Classify this cell by malaria status.
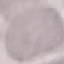

It is uninfected.

Summary:
  - Stain: Giemsa
  - Capture: smartphone camera at the microscope eyepiece
  - Preparation: thin blood smear
  - Image type: automatically extracted cell patch, resized to 64 × 64 pixels